State which parasite is depicted.
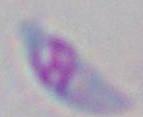

Toxoplasma gondii.

modality = micrograph
magnification = 1000x